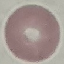

Summary:
  - Malaria status: uninfected
  - Preparation: thin smear
  - Capture: smartphone camera at the microscope eyepiece
  - Stain: Giemsa
  - Image type: automatically extracted cell patch, resized to 64 × 64 pixels